Comment on the morphology of the erythrocytes.
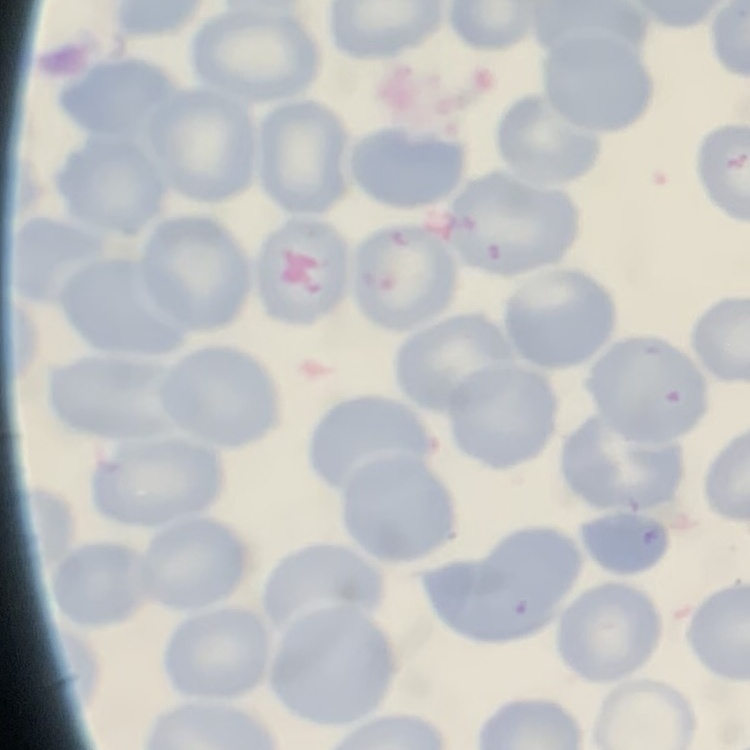
No rouleaux formation.

Summary:
  - Preparation: thin blood smear
  - Stain: Field's or Giemsa
  - Image type: square crop of a larger photomicrograph